Point out each Plasmodium parasite and each leukocyte.
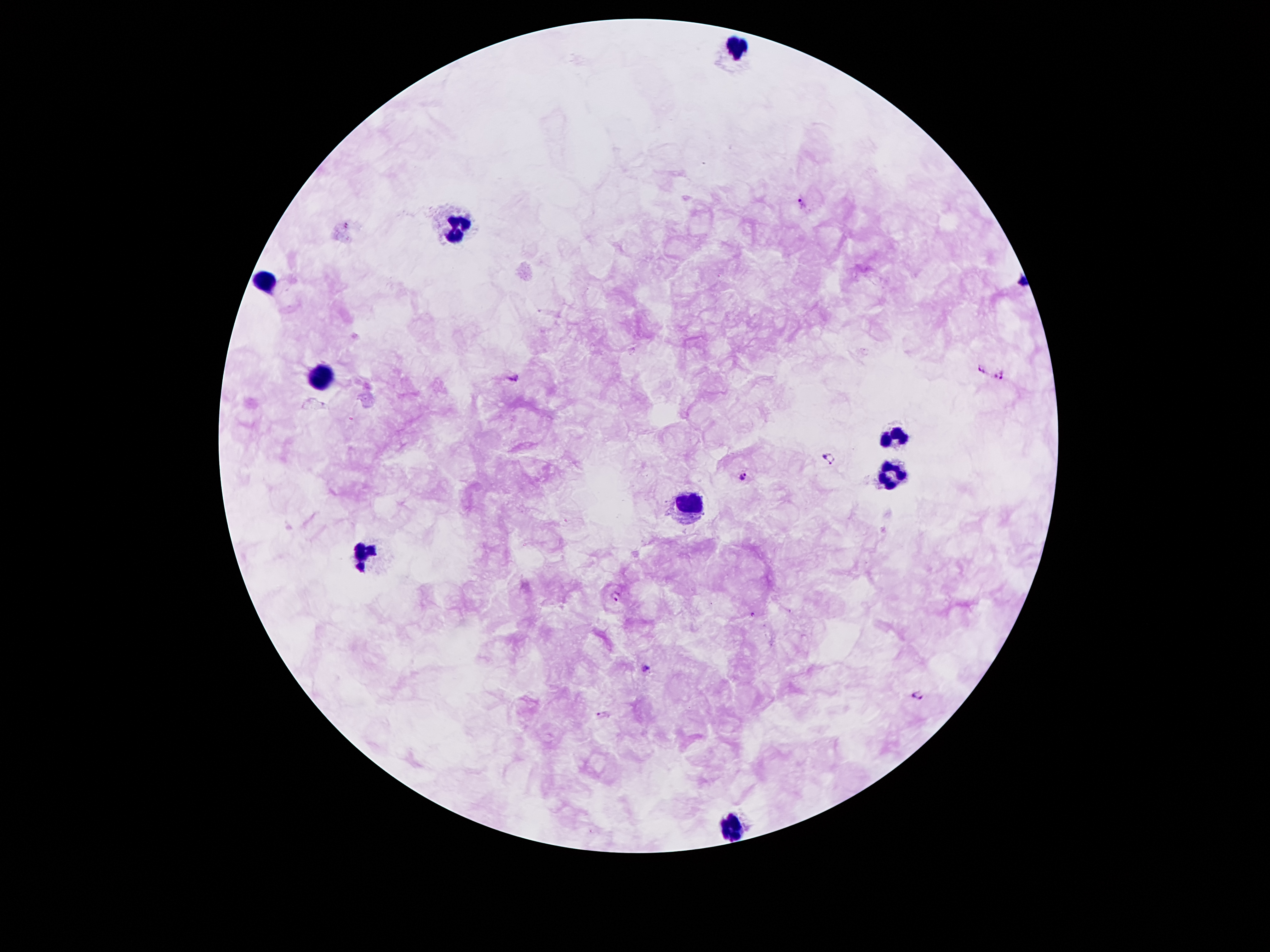

Approximate centers as {x, y} in pixels.
Plasmodium parasites: {802, 205}, {982, 368}, {516, 376}, {999, 377}, {829, 457}, {742, 476}, {617, 598}, {649, 669}, {919, 696}, {605, 714}.
Leukocytes: {735, 45}, {454, 225}, {267, 281}, {322, 378}, {894, 439}, {887, 474}, {690, 499}, {361, 554}, {729, 822}.

image size = 1270×952 pixels
capture = smartphone through the microscope eyepiece
preparation = thick peripheral-blood smear
field of view = one from this slide
stain = Giemsa
magnification = 100x
patient malaria status = positive for Plasmodium falciparum